Name the cell type shown.
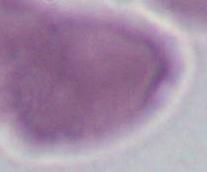
An erythrocyte.

magnification = 1000x
modality = photomicrograph